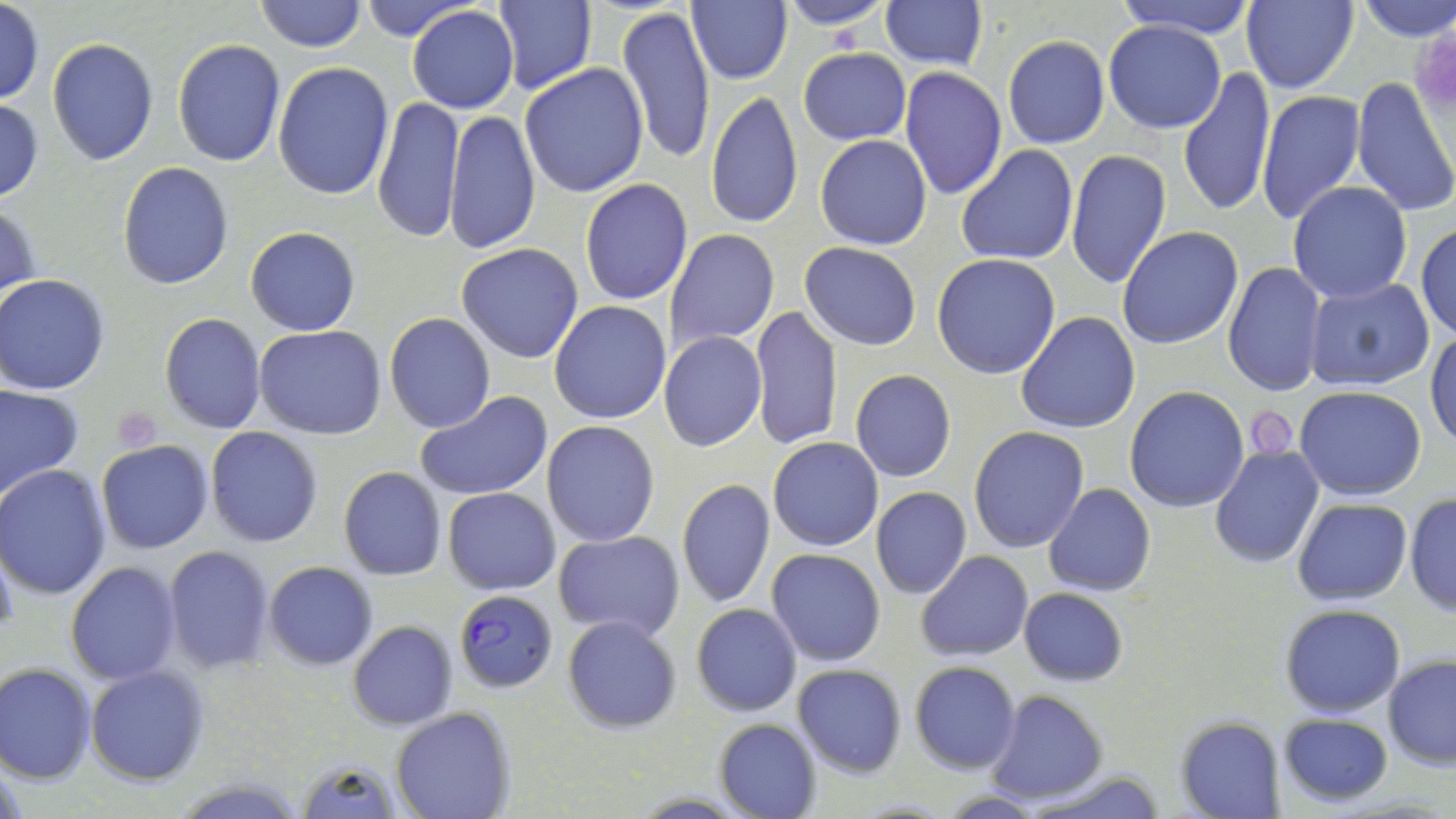

Summary:
  - Coordinate format: approximate bounding boxes as [x1, y1, x2, y2] in pixels
  - Plasmodium falciparum-infected red blood cell locations: [453, 590, 557, 692]
  - Uninfected red blood cell locations: [253, 0, 368, 52], [356, 0, 482, 45], [492, 0, 596, 95], [687, 0, 792, 86], [773, 0, 896, 29], [880, 0, 986, 70], [1111, 0, 1259, 38], [1240, 0, 1359, 93], [1351, 0, 1456, 41], [0, 2, 45, 105], [617, 4, 717, 167], [406, 6, 520, 114], [1102, 21, 1228, 134], [1003, 37, 1110, 149], [46, 38, 159, 167], [170, 40, 287, 168], [798, 46, 911, 146], [272, 61, 394, 201], [519, 64, 649, 198], [899, 67, 1005, 199], [1177, 67, 1277, 218], [1351, 76, 1456, 217], [1256, 90, 1365, 226], [706, 92, 802, 229], [373, 95, 464, 245], [0, 98, 45, 203], [446, 109, 541, 256], [814, 135, 932, 251], [956, 145, 1079, 267], [1065, 149, 1172, 290], [117, 162, 234, 290], [580, 178, 693, 306], [1287, 182, 1413, 304], [0, 198, 43, 309], [1414, 223, 1456, 341], [245, 227, 360, 336], [1116, 227, 1243, 350], [665, 229, 779, 351], [800, 242, 921, 350], [456, 243, 584, 364], [932, 254, 1060, 378], [1222, 261, 1327, 398], [1, 276, 109, 394], [1305, 278, 1435, 391], [548, 300, 671, 424], [750, 305, 843, 452], [1016, 311, 1140, 434], [383, 312, 496, 435], [159, 313, 267, 435], [254, 326, 387, 440], [1425, 330, 1456, 450], [658, 332, 767, 452], [850, 369, 957, 482], [0, 384, 82, 501], [1125, 386, 1249, 513], [1294, 386, 1426, 499], [414, 391, 555, 503], [541, 420, 660, 546], [969, 425, 1088, 552], [205, 426, 325, 548], [768, 437, 883, 552], [96, 440, 213, 553], [1210, 446, 1324, 568], [1, 465, 114, 599], [338, 466, 447, 580], [676, 478, 775, 608], [1045, 484, 1155, 597], [871, 486, 972, 599], [444, 487, 562, 594], [1405, 492, 1456, 617], [1293, 498, 1411, 605], [552, 531, 684, 641], [0, 538, 19, 641], [161, 544, 276, 674], [767, 548, 887, 666], [917, 551, 1034, 660], [265, 561, 378, 669], [64, 563, 182, 685], [1019, 588, 1128, 685], [690, 603, 802, 717], [1277, 604, 1405, 717], [562, 614, 682, 733], [348, 621, 457, 731], [1383, 654, 1456, 769], [909, 661, 1021, 774], [1, 662, 97, 785], [791, 664, 906, 778], [85, 665, 209, 785], [985, 691, 1107, 804], [391, 708, 513, 819], [1276, 712, 1394, 806], [1174, 716, 1285, 819], [715, 719, 821, 819], [289, 756, 408, 818], [1023, 768, 1169, 819]
  - Platelet locations: [110, 408, 161, 453], [1249, 411, 1298, 459]
  - Slide-level diagnosis: Plasmodium falciparum
  - Magnification: 1000x
  - Modality: light microscopy
  - Image size: 1456×819 pixels
  - Stain: May-Grünwald-Giemsa
  - Field of view: single
  - Preparation: thin blood film